Classify this cell by malaria status.
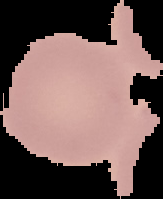
It is uninfected.

{
  "image_size": "163×199 pixels",
  "image_type": "segmented cell region with the area outside set to black",
  "preparation": "thin blood smear"
}